Identify the preparation type.
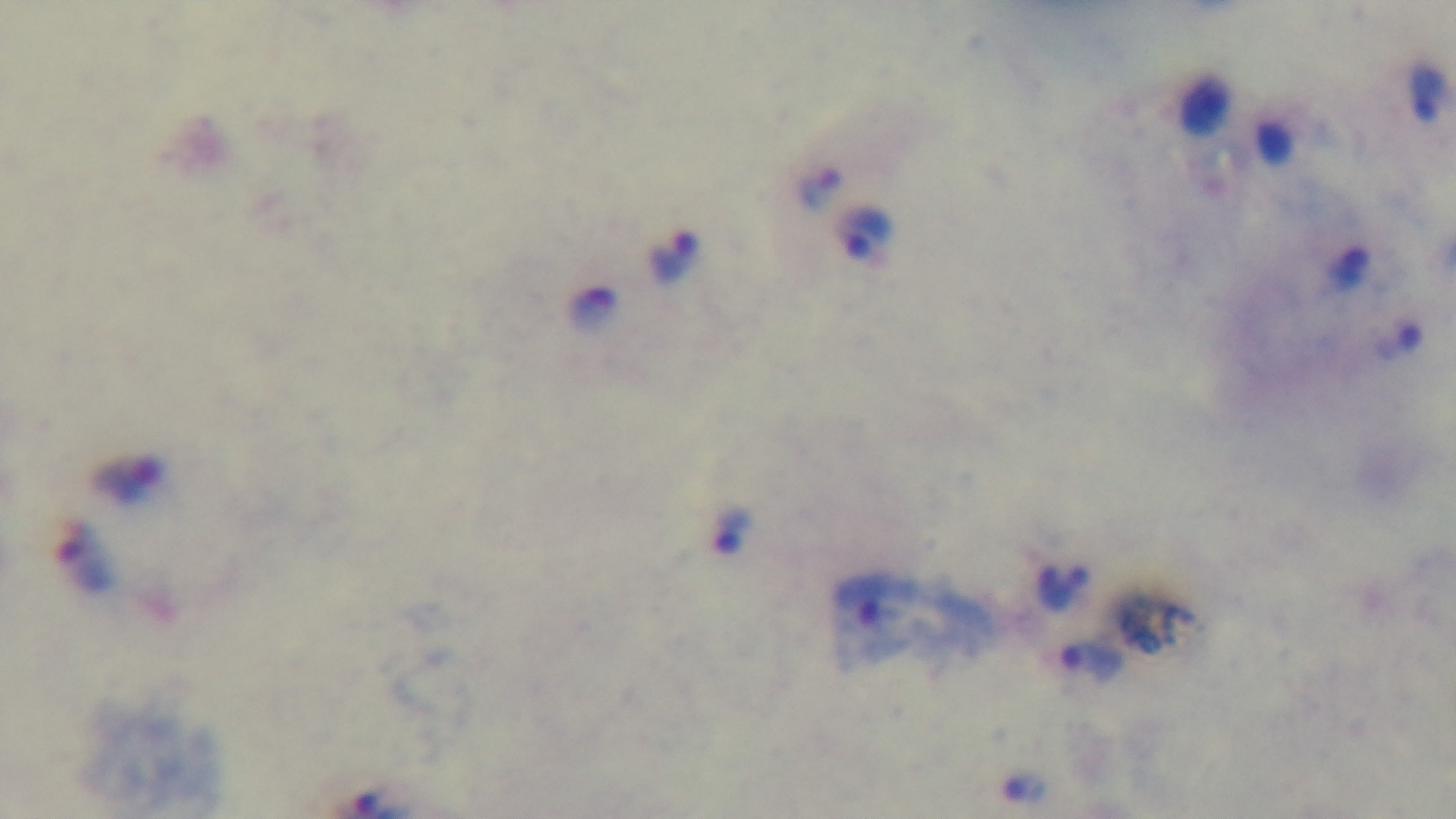

It is a thick blood film.

Summary:
  - Objective: 100x oil immersion
  - Capture: mounted 4K digital camera
  - Field of view: single
  - Stain: Giemsa
  - Modality: light microscopy
  - Malaria status: positive